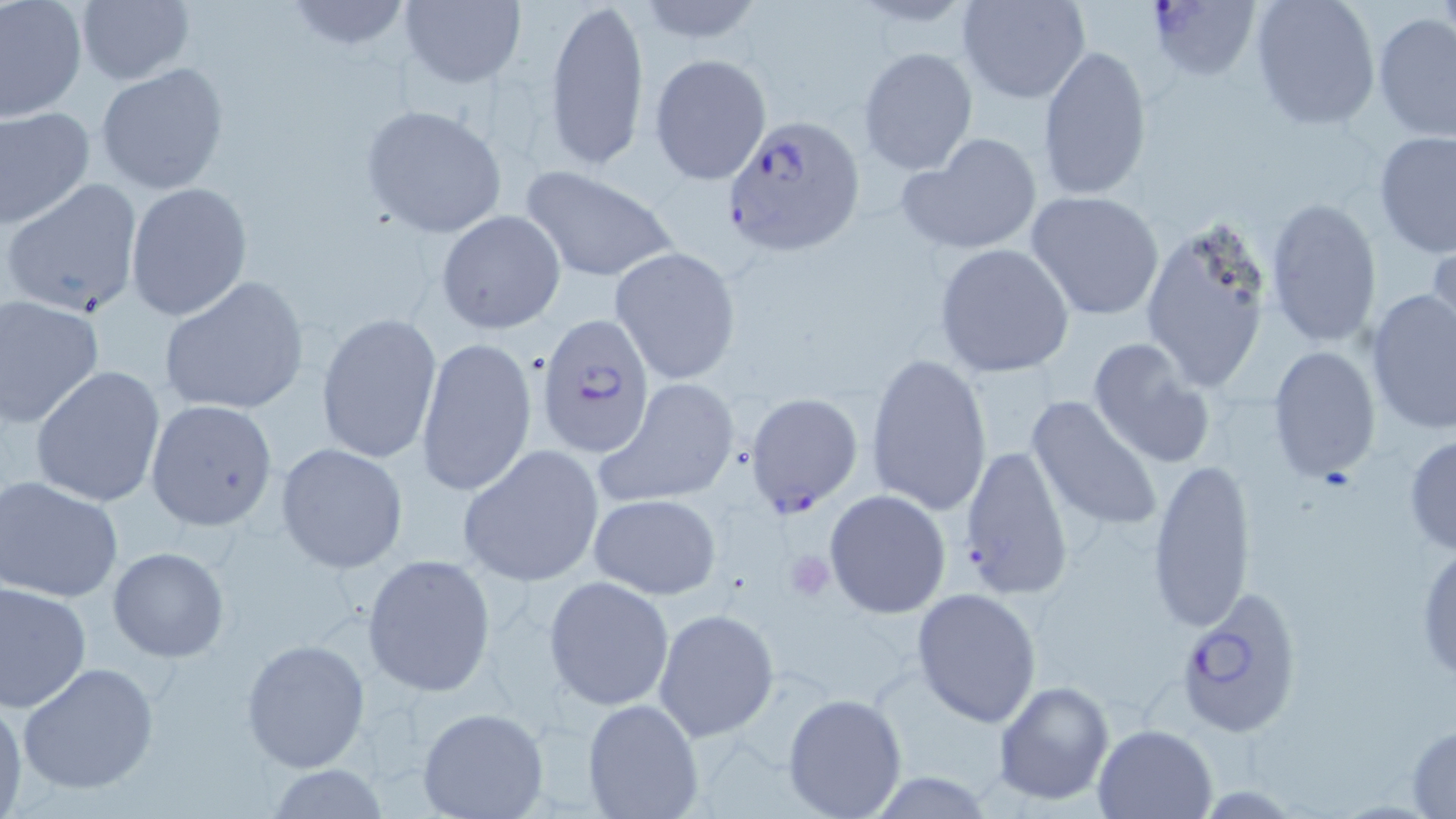

Summary:
  - Coordinate format: approximate bounding boxes as [x1, y1, x2, y2] in pixels
  - Uninfected red blood cell locations: [0, 0, 88, 122], [280, 0, 415, 52], [547, 0, 651, 171], [958, 0, 1091, 104], [1247, 0, 1380, 131], [399, 1, 525, 88], [630, 1, 771, 49], [75, 2, 194, 85], [1371, 12, 1455, 141], [1036, 44, 1153, 203], [858, 47, 977, 175], [649, 53, 772, 185], [97, 63, 230, 196], [359, 103, 507, 239], [0, 105, 95, 230], [1373, 131, 1456, 261], [898, 132, 1044, 257], [520, 165, 680, 284], [2, 177, 143, 320], [125, 181, 253, 322], [1024, 190, 1167, 322], [1263, 197, 1384, 349], [436, 211, 566, 334], [1135, 218, 1279, 396], [1428, 239, 1456, 350], [933, 242, 1076, 379], [610, 247, 741, 385], [157, 276, 310, 418], [1365, 286, 1456, 435], [0, 295, 107, 432], [315, 311, 442, 464], [416, 334, 536, 501], [1087, 336, 1214, 468], [1267, 345, 1382, 481], [865, 353, 993, 520], [29, 365, 168, 507], [597, 380, 741, 509], [1025, 394, 1165, 537], [144, 400, 277, 531], [1403, 434, 1456, 557], [277, 443, 407, 575], [458, 444, 606, 588], [1146, 456, 1257, 636], [0, 477, 125, 605], [823, 488, 952, 619], [590, 493, 723, 600], [1415, 537, 1456, 686], [107, 547, 230, 664], [361, 553, 497, 697], [543, 575, 675, 711], [0, 580, 94, 714], [911, 587, 1043, 728], [652, 609, 778, 740], [241, 637, 370, 772], [18, 662, 161, 796], [993, 679, 1115, 805], [782, 692, 907, 819], [0, 696, 26, 816], [582, 698, 706, 819], [416, 708, 549, 819], [1093, 722, 1217, 818], [1406, 723, 1456, 817], [264, 765, 392, 818]
  - Platelet locations: [782, 551, 836, 600]
  - Plasmodium falciparum-infected red blood cell locations: [1145, 0, 1262, 86], [723, 116, 867, 257], [535, 311, 656, 456], [746, 392, 864, 516], [957, 444, 1073, 599], [1174, 587, 1305, 739]
  - Slide-level diagnosis: Plasmodium falciparum
  - Image size: 1456×819 pixels
  - Modality: optical microscopy
  - Field of view: one of a larger specimen
  - Stain: May-Grünwald-Giemsa
  - Magnification: 1000x
  - Preparation: thin blood film